Report the malaria status of this cell.
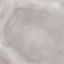

Uninfected.

preparation = thin smear
capture = smartphone through the microscope eyepiece
image type = cell patch, automatically extracted from a larger field of view and resized to 64 × 64 pixels
stain = Giemsa